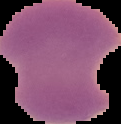
Summary:
  - Preparation: thin blood film
  - Malaria status: parasitized
  - Image size: 121×124 pixels
  - Image type: segmented cell region on a black background